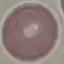
Summary:
  - Result: no malaria parasites seen
  - Capture: smartphone camera at the microscope eyepiece
  - Stain: Giemsa
  - Preparation: thin blood film
  - Image type: automatically extracted cell patch, resized to 64 × 64 pixels